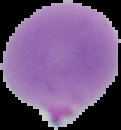
Summary:
  - Image size: 121×130 pixels
  - Preparation: thin blood film
  - Malaria status: parasitized
  - Image type: segmented cell region with the area outside set to black